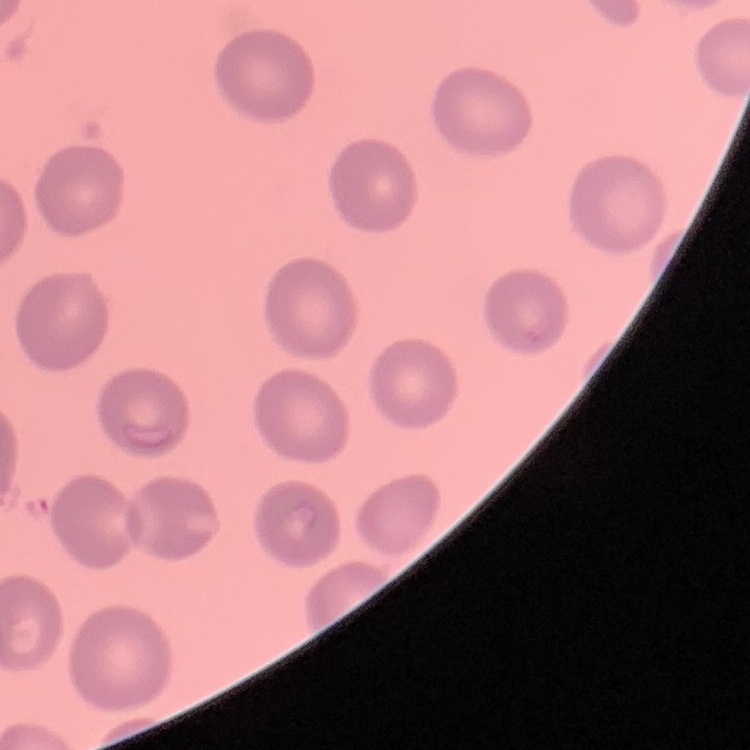

The red blood cells show no rouleaux formation. Stained with either Field's or Giemsa. Thin peripheral smear. One tile cut from a larger photomicrograph.